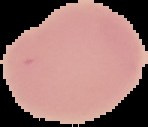
result = negative for Plasmodium parasites
image size = 148×127 pixels
preparation = thin blood film
image type = cell region segmented out of the field of view; surrounding area masked to black